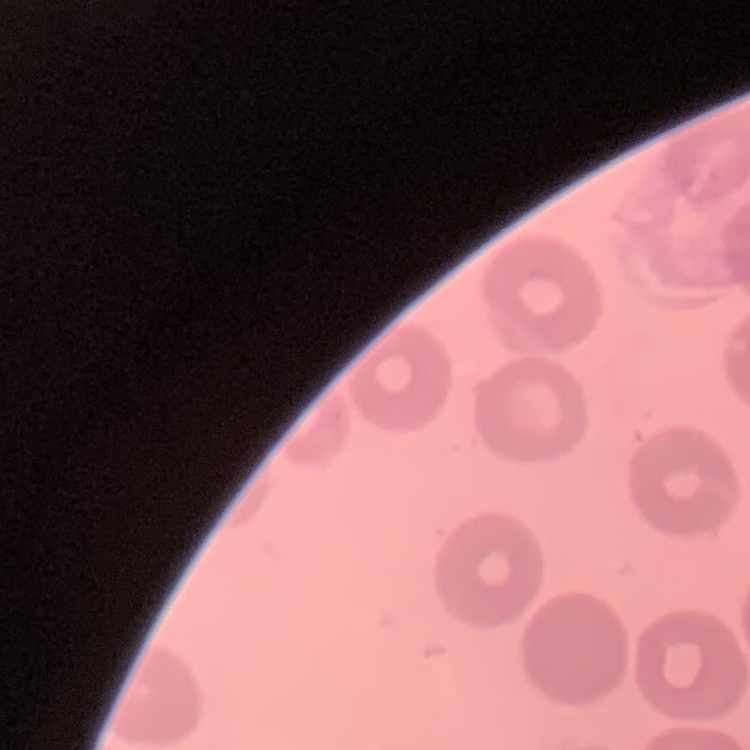

erythrocyte morphology = no rouleaux formation
preparation = thin blood film
stain = Field's or Giemsa
image type = square crop of a larger photomicrograph